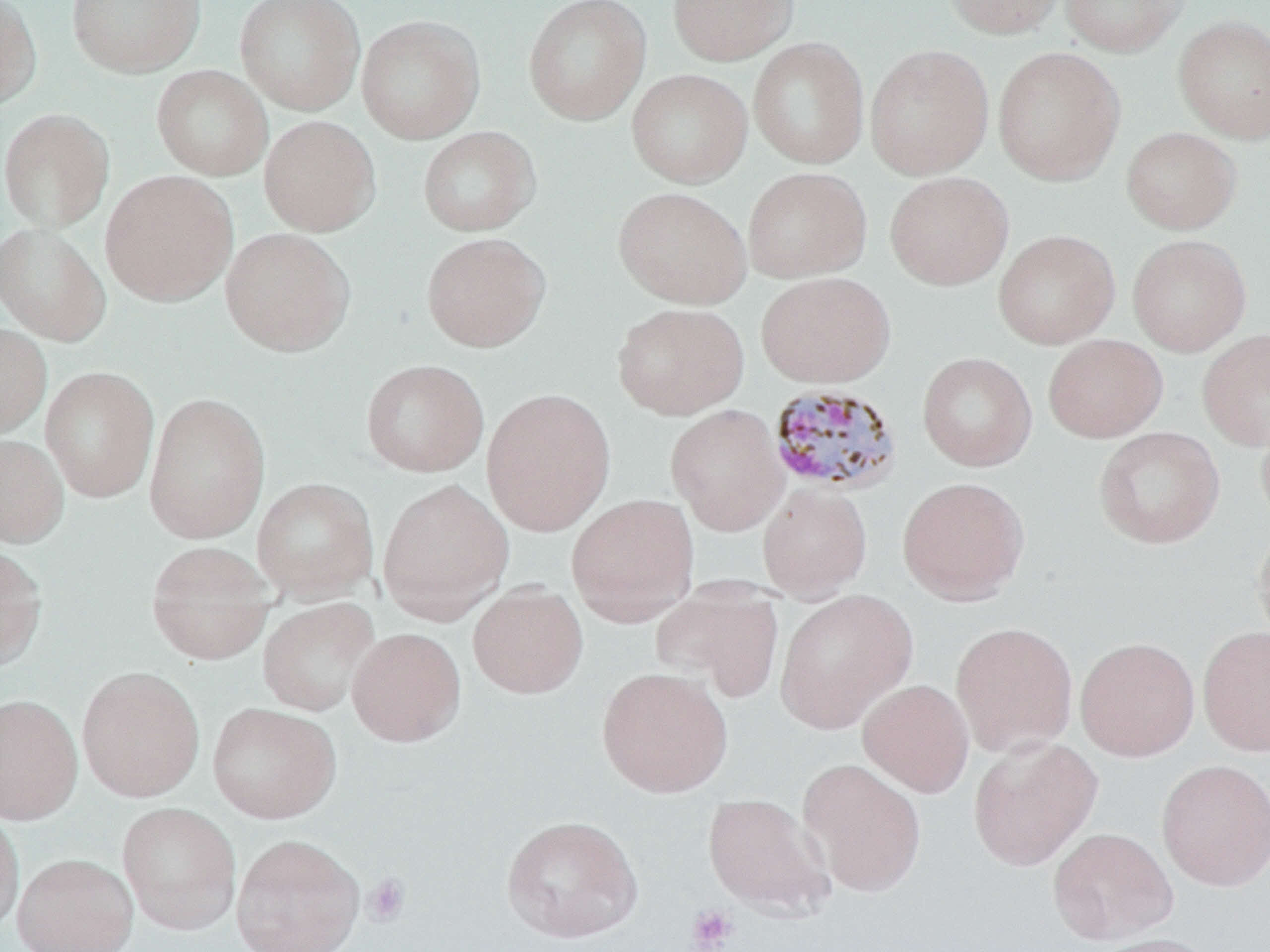 Approximate bounding boxes as [x1, y1, x2, y2] in pixels. Plasmodium malariae-infected red blood cell locations: [771, 385, 906, 497]. Uninfected red blood cell locations: [0, 0, 42, 111], [66, 0, 206, 79], [234, 0, 366, 115], [522, 0, 652, 126], [667, 0, 798, 66], [942, 0, 1067, 38], [1059, 0, 1191, 57], [356, 14, 485, 144], [1172, 14, 1270, 144], [747, 37, 869, 170], [864, 43, 995, 180], [992, 45, 1126, 186], [151, 65, 273, 180], [626, 68, 753, 189], [0, 108, 115, 233], [258, 115, 381, 237], [417, 126, 540, 237], [1121, 126, 1242, 234], [742, 166, 872, 283], [99, 170, 239, 307], [884, 171, 1014, 290], [612, 186, 752, 309], [0, 222, 111, 346], [219, 227, 355, 357], [992, 229, 1121, 349], [421, 232, 551, 352], [1126, 233, 1252, 356], [755, 271, 896, 388], [611, 302, 750, 420], [0, 322, 52, 441], [1196, 328, 1270, 452], [1042, 334, 1168, 443], [916, 351, 1037, 472], [360, 359, 489, 477], [39, 365, 160, 503], [480, 387, 617, 537], [142, 390, 271, 544], [665, 404, 789, 536], [1255, 405, 1270, 532], [1093, 426, 1225, 549], [0, 432, 68, 548], [896, 476, 1030, 605], [250, 477, 379, 603], [376, 479, 514, 621], [757, 482, 873, 599], [566, 493, 699, 626], [1252, 522, 1270, 649], [145, 540, 276, 665], [0, 542, 48, 673], [467, 582, 589, 699], [650, 584, 784, 704], [773, 590, 916, 733], [257, 597, 380, 717], [950, 621, 1079, 757], [1197, 625, 1270, 756], [346, 627, 467, 747], [1075, 636, 1200, 761], [76, 665, 206, 802], [596, 666, 734, 798], [858, 679, 975, 797], [0, 693, 83, 824], [206, 701, 341, 824], [967, 735, 1103, 871], [798, 757, 927, 897], [1156, 758, 1270, 891], [702, 792, 834, 918], [117, 802, 242, 935], [0, 808, 24, 935], [500, 814, 644, 943], [1047, 827, 1178, 945], [230, 833, 365, 952], [12, 852, 139, 952], [1089, 932, 1224, 952]. Platelet locations: [362, 873, 411, 927], [686, 904, 739, 951]. Slide-level diagnosis: Plasmodium malariae. May-Grünwald-Giemsa-stained preparation. 1000x magnification. Thin blood film. Optical microscopy. One field of a larger specimen. Image is 1270×952 pixels.